Report the malaria status of this cell.
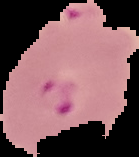

Parasitized.

Segmented cell region on a black background. From a thin blood film. Image is 139×157 pixels.